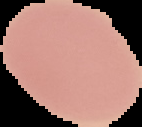

Summary:
  - Preparation: thin blood smear
  - Image type: segmented cell region with the area outside set to black
  - Malaria status: uninfected
  - Image size: 142×127 pixels